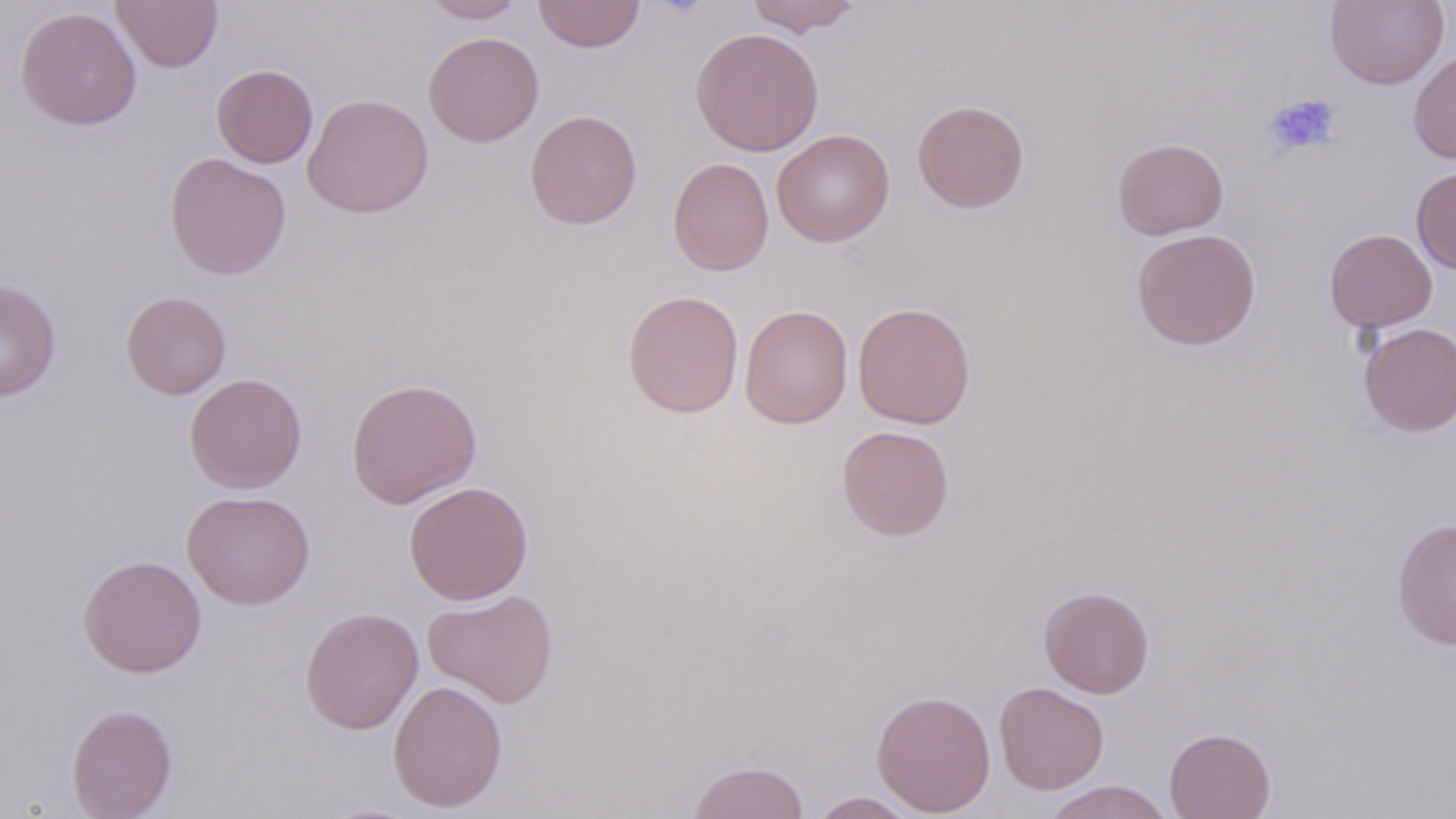
Summary:
  - Coordinate format: approximate bounding boxes as named x1/y1/x2/y2 corners in pixels
  - Platelet locations: (x1=1264, y1=93, x2=1341, y2=158)
  - Uninfected red blood cell locations: (x1=112, y1=0, x2=223, y2=72), (x1=419, y1=0, x2=529, y2=22), (x1=532, y1=0, x2=647, y2=53), (x1=745, y1=0, x2=863, y2=36), (x1=1325, y1=0, x2=1450, y2=90), (x1=15, y1=6, x2=142, y2=131), (x1=689, y1=27, x2=825, y2=156), (x1=423, y1=31, x2=544, y2=147), (x1=1408, y1=47, x2=1456, y2=164), (x1=211, y1=64, x2=318, y2=168), (x1=302, y1=93, x2=433, y2=218), (x1=911, y1=99, x2=1030, y2=213), (x1=525, y1=110, x2=642, y2=230), (x1=771, y1=129, x2=894, y2=247), (x1=1113, y1=137, x2=1229, y2=240), (x1=164, y1=153, x2=291, y2=279), (x1=668, y1=157, x2=774, y2=276), (x1=1411, y1=167, x2=1456, y2=274), (x1=1131, y1=228, x2=1261, y2=350), (x1=1324, y1=229, x2=1437, y2=332), (x1=0, y1=279, x2=60, y2=401), (x1=622, y1=290, x2=744, y2=418), (x1=121, y1=291, x2=231, y2=399), (x1=852, y1=302, x2=976, y2=429), (x1=739, y1=304, x2=852, y2=429), (x1=1358, y1=322, x2=1456, y2=436), (x1=184, y1=373, x2=307, y2=494), (x1=346, y1=377, x2=483, y2=508), (x1=837, y1=425, x2=955, y2=541), (x1=404, y1=481, x2=533, y2=605), (x1=181, y1=490, x2=315, y2=610), (x1=1392, y1=518, x2=1456, y2=649), (x1=77, y1=555, x2=206, y2=678), (x1=1038, y1=585, x2=1155, y2=698), (x1=422, y1=589, x2=559, y2=708), (x1=299, y1=607, x2=423, y2=734), (x1=387, y1=679, x2=507, y2=813), (x1=994, y1=682, x2=1109, y2=794), (x1=871, y1=690, x2=996, y2=816), (x1=66, y1=703, x2=177, y2=819), (x1=1164, y1=727, x2=1276, y2=819), (x1=686, y1=760, x2=810, y2=819), (x1=1042, y1=781, x2=1174, y2=819), (x1=807, y1=792, x2=921, y2=818)
  - Slide-level diagnosis: negative for blood parasites
  - Magnification: 1000x
  - Preparation: thin blood smear
  - Image size: 1456×819 pixels
  - Field of view: one of a larger specimen
  - Stain: May-Grünwald-Giemsa
  - Modality: light microscopy